State which cell type is depicted.
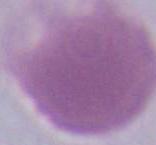

An erythrocyte.

Captured at 1000x magnification. Micrograph.